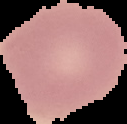
preparation = thin blood smear
image size = 127×124 pixels
image type = cell region segmented out of the field of view; surrounding area masked to black
result = negative for malaria parasites